Assess this cell for malaria.
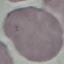
Uninfected.

preparation = thin smear
image type = cell patch, automatically extracted from a larger field of view and resized to 64 × 64 pixels
capture = smartphone through the microscope eyepiece
stain = Giemsa